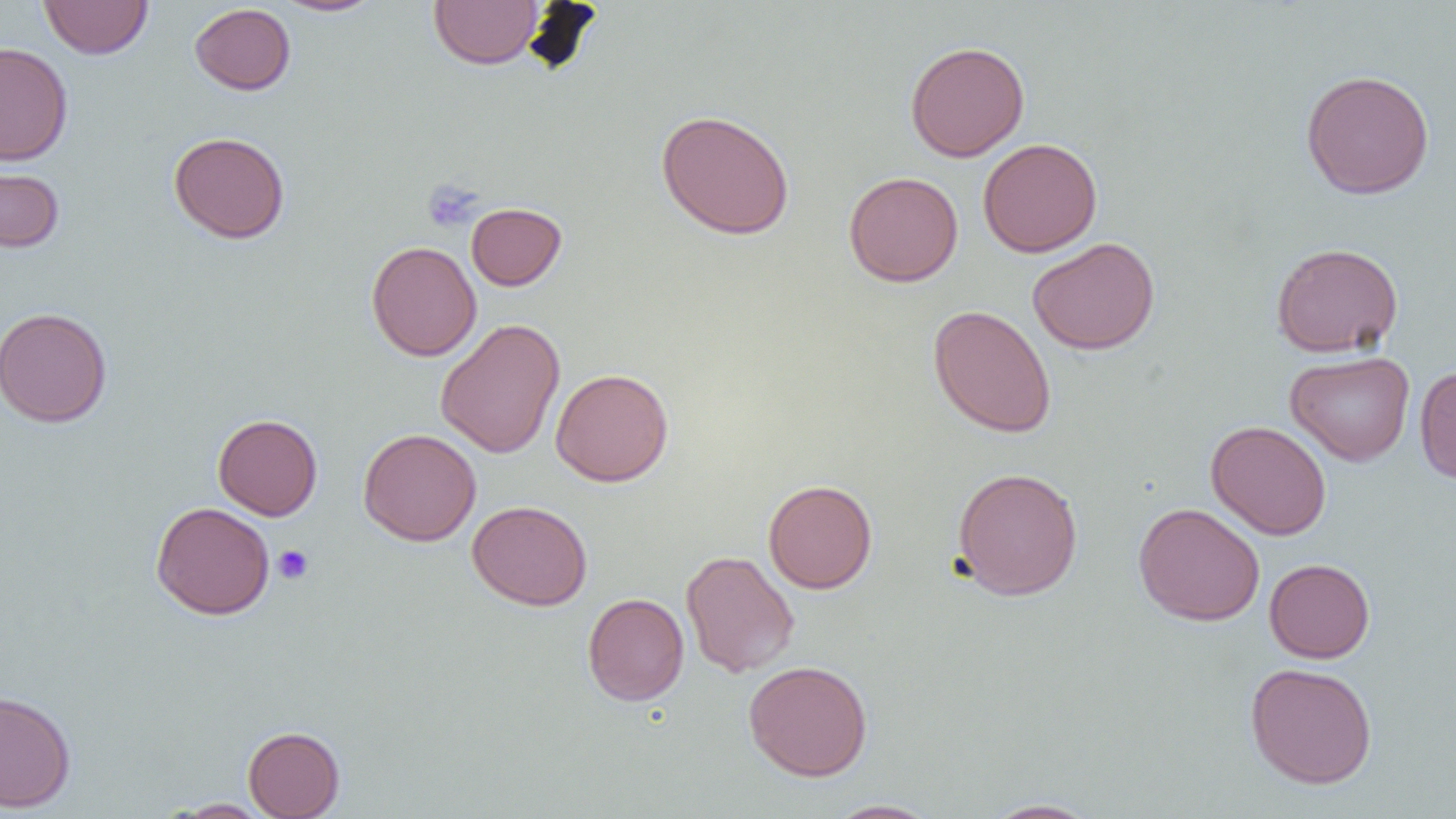

Approximate bounding boxes as [x1, y1, x2, y2] in pixels. Platelet locations: [422, 180, 483, 232], [273, 545, 314, 585]. Uninfected red blood cell locations: [39, 0, 153, 59], [272, 0, 386, 17], [429, 0, 543, 70], [189, 3, 296, 95], [0, 41, 73, 165], [904, 41, 1030, 162], [1300, 69, 1435, 200], [656, 109, 795, 240], [168, 131, 291, 244], [978, 138, 1102, 257], [0, 164, 65, 253], [843, 171, 963, 287], [466, 202, 566, 290], [1027, 237, 1160, 355], [366, 241, 482, 361], [1271, 242, 1403, 358], [928, 304, 1056, 438], [0, 306, 112, 428], [435, 318, 565, 459], [1285, 350, 1415, 465], [1414, 365, 1456, 485], [550, 368, 674, 487], [213, 414, 322, 521], [1206, 420, 1332, 540], [358, 428, 481, 546], [951, 467, 1084, 600], [763, 479, 878, 594], [467, 500, 593, 610], [151, 501, 275, 620], [1133, 502, 1265, 626], [681, 550, 800, 678], [1264, 558, 1375, 663], [582, 592, 689, 705], [743, 660, 873, 781], [1245, 661, 1378, 789], [0, 688, 77, 812], [243, 725, 345, 818], [165, 798, 274, 817], [979, 798, 1102, 818], [825, 799, 941, 818]. Slide-level diagnosis: negative for blood parasites. Image is 1456×819 pixels. 1000x magnification. Thin blood film. One field of a larger specimen. Light microscopy.